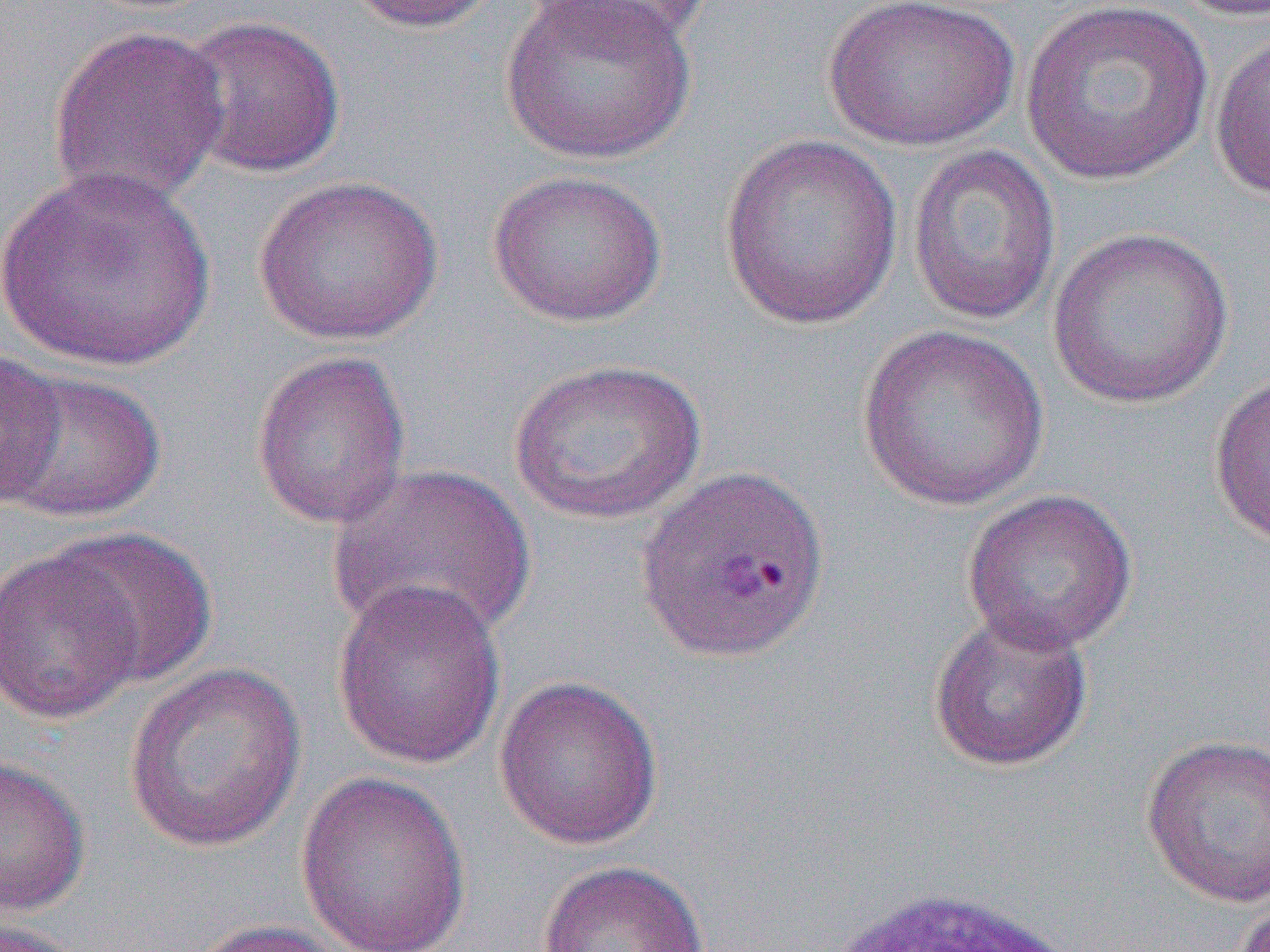
slide-level diagnosis = Plasmodium vivax
image size = 1270×952 pixels
preparation = thin blood film
field of view = single
uninfected red blood cell locations = approximate bounding boxes as named x1/y1/x2/y2 corners in pixels: (x1=340, y1=0, x2=504, y2=34), (x1=497, y1=0, x2=699, y2=167), (x1=521, y1=0, x2=712, y2=49), (x1=823, y1=0, x2=1020, y2=151), (x1=1020, y1=0, x2=1214, y2=186), (x1=1167, y1=0, x2=1270, y2=22), (x1=174, y1=14, x2=348, y2=179), (x1=46, y1=24, x2=230, y2=211), (x1=1208, y1=26, x2=1270, y2=204), (x1=718, y1=133, x2=904, y2=330), (x1=907, y1=144, x2=1062, y2=326), (x1=1, y1=164, x2=216, y2=372), (x1=486, y1=168, x2=667, y2=327), (x1=252, y1=174, x2=444, y2=346), (x1=1045, y1=226, x2=1235, y2=410), (x1=855, y1=324, x2=1051, y2=512), (x1=250, y1=349, x2=412, y2=530), (x1=0, y1=350, x2=65, y2=506), (x1=508, y1=358, x2=707, y2=526), (x1=2, y1=368, x2=166, y2=525), (x1=1208, y1=372, x2=1270, y2=549), (x1=325, y1=462, x2=536, y2=646), (x1=962, y1=488, x2=1138, y2=654), (x1=52, y1=526, x2=217, y2=690), (x1=0, y1=544, x2=146, y2=727), (x1=331, y1=578, x2=506, y2=770), (x1=927, y1=609, x2=1095, y2=773), (x1=122, y1=661, x2=307, y2=854), (x1=493, y1=675, x2=664, y2=850), (x1=1140, y1=734, x2=1270, y2=909), (x1=0, y1=754, x2=91, y2=915), (x1=295, y1=771, x2=472, y2=952), (x1=537, y1=859, x2=709, y2=952), (x1=1229, y1=896, x2=1270, y2=952), (x1=186, y1=918, x2=354, y2=952), (x1=0, y1=919, x2=92, y2=952)
white blood cell locations = approximate bounding boxes as named x1/y1/x2/y2 corners in pixels: (x1=825, y1=886, x2=1083, y2=952)
magnification = 1000x
modality = light microscopy